State which cell type is depicted.
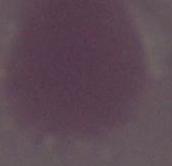
This is an erythrocyte.

1000x magnification. Micrograph.